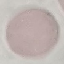

malaria_status: uninfected
preparation: thin blood film
capture: smartphone camera at the microscope eyepiece
stain: Giemsa
image_type: cell patch, automatically extracted from a larger field of view and resized to 64 × 64 pixels